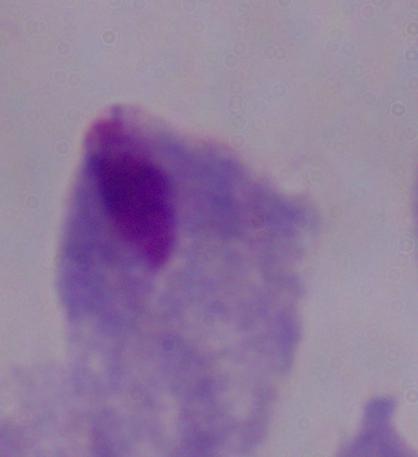
Summary:
  - Modality: micrograph
  - Identification: trichomonad
  - Magnification: 1000x